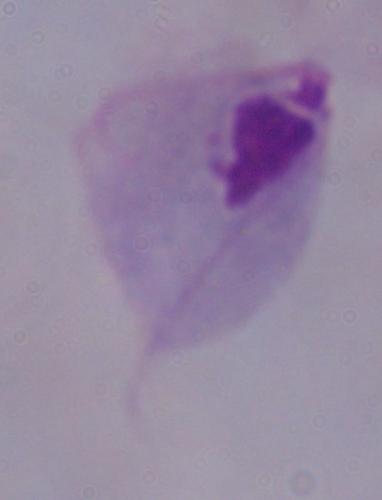

magnification: 1000x
modality: micrograph
identification: trichomonad